Name the blood parasite species.
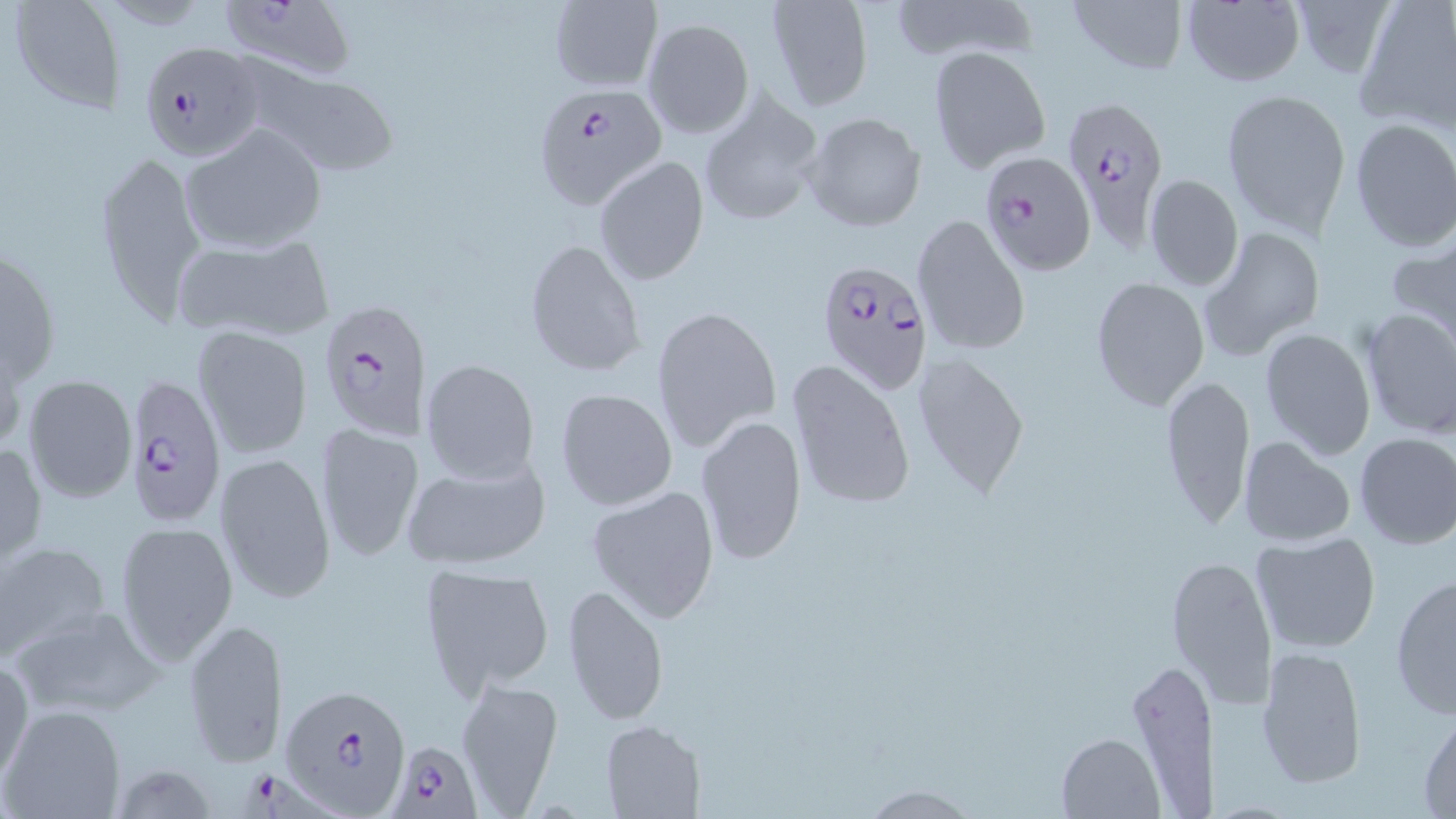
Plasmodium falciparum.

preparation: thin blood film
uninfected_red_blood_cell_locations: 'approximate bounding boxes as (x1,y1)-(x2,y2) corner pairs in pixels: (8,0)-(124,112), (888,0)-(1034,66), (1065,0)-(1189,75), (1181,0)-(1306,87), (547,1)-(662,91), (763,1)-(873,112), (1355,2)-(1456,131), (643,18)-(753,139), (927,45)-(1051,173), (233,59)-(403,177), (1220,88)-(1352,238), (695,93)-(825,227), (804,111)-(926,232), (1348,118)-(1456,253), (180,123)-(326,251), (92,151)-(207,324), (594,156)-(708,284), (1144,174)-(1243,291), (912,214)-(1031,358), (1200,226)-(1326,362), (168,231)-(336,343), (1386,235)-(1456,348), (0,236)-(62,397), (523,237)-(645,377), (1090,275)-(1210,411), (651,304)-(781,454), (1359,307)-(1456,440), (192,326)-(313,459), (1259,328)-(1375,460), (910,351)-(1030,501), (419,357)-(541,484), (787,360)-(914,514), (22,374)-(136,503), (1159,374)-(1256,531), (555,387)-(678,511), (695,415)-(807,564), (315,421)-(423,563), (1353,432)-(1456,550), (1237,436)-(1357,547), (0,440)-(47,569), (214,452)-(336,604), (399,453)-(553,571), (585,484)-(720,623), (574,503)-(697,704), (114,522)-(237,665), (1250,530)-(1383,655), (0,542)-(112,661), (1167,552)-(1279,709), (417,562)-(556,697), (1388,573)-(1455,719), (562,583)-(670,727), (8,602)-(166,722), (184,617)-(287,771), (1255,643)-(1369,790), (1,653)-(33,789), (453,677)-(564,812), (0,705)-(126,818), (1416,708)-(1456,814), (600,721)-(706,819), (1057,731)-(1163,817), (119,760)-(216,819), (862,783)-(979,818)'
modality: optical microscopy
magnification: 1000x
image_size: 1456×819 pixels
field_of_view: one of a larger specimen
stain: May-Grünwald-Giemsa
plasmodium_falciparum_infected_red_blood_cell_locations: 'approximate bounding boxes as (x1,y1)-(x2,y2) corner pairs in pixels: (224,4)-(361,79), (149,41)-(267,169), (536,83)-(666,210), (1063,97)-(1170,243), (977,151)-(1098,277), (813,255)-(934,397), (315,302)-(433,436), (123,373)-(225,532), (279,683)-(411,812), (388,739)-(481,817), (240,770)-(335,819)'